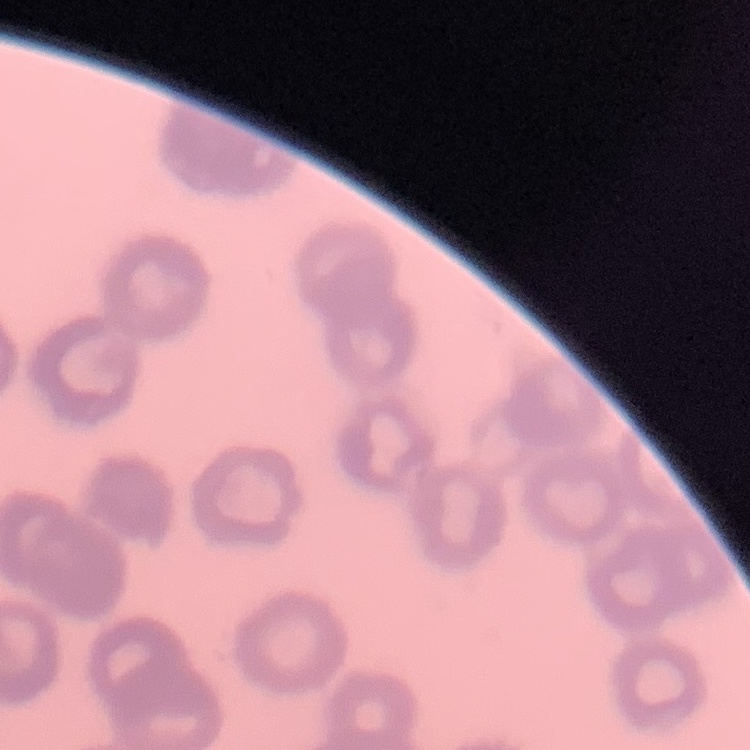

The red blood cells show rouleaux formation. One tile cut from a larger photomicrograph. Stained with either Field's or Giemsa. Thin blood film.